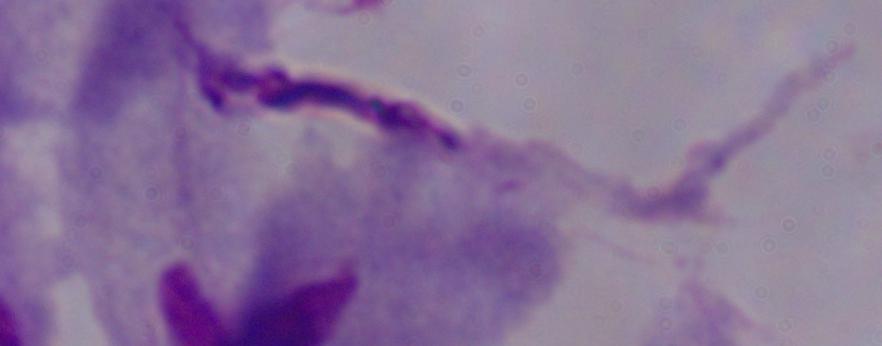

Summary:
  - Magnification: 1000x
  - Modality: photomicrograph
  - Identification: trichomonad